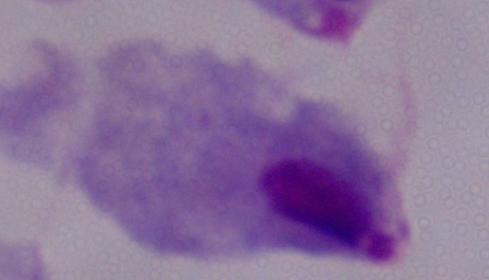

Summary:
  - Magnification: 1000x
  - Identification: trichomonad
  - Modality: micrograph